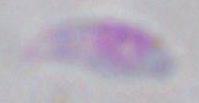
Micrograph. Captured at 1000x magnification. Toxoplasma gondii is shown.